Assess the morphology of the erythrocytes.
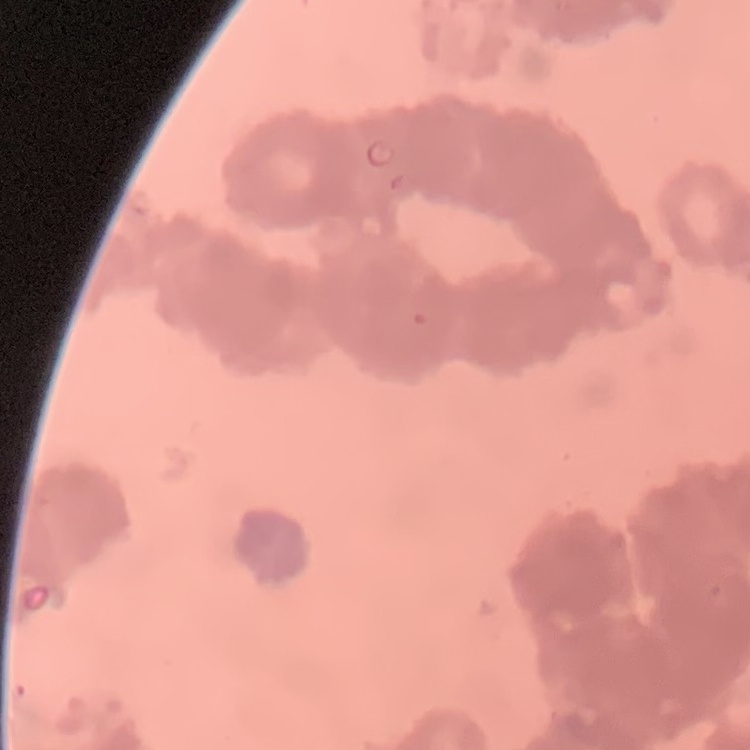
Rouleaux formation.

Summary:
  - Image type: one tile cut from a larger photomicrograph
  - Preparation: thin blood smear
  - Stain: Field's or Giemsa